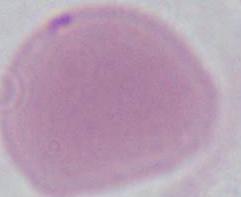
{
  "identification": "red blood cell",
  "magnification": "1000x",
  "modality": "micrograph"
}